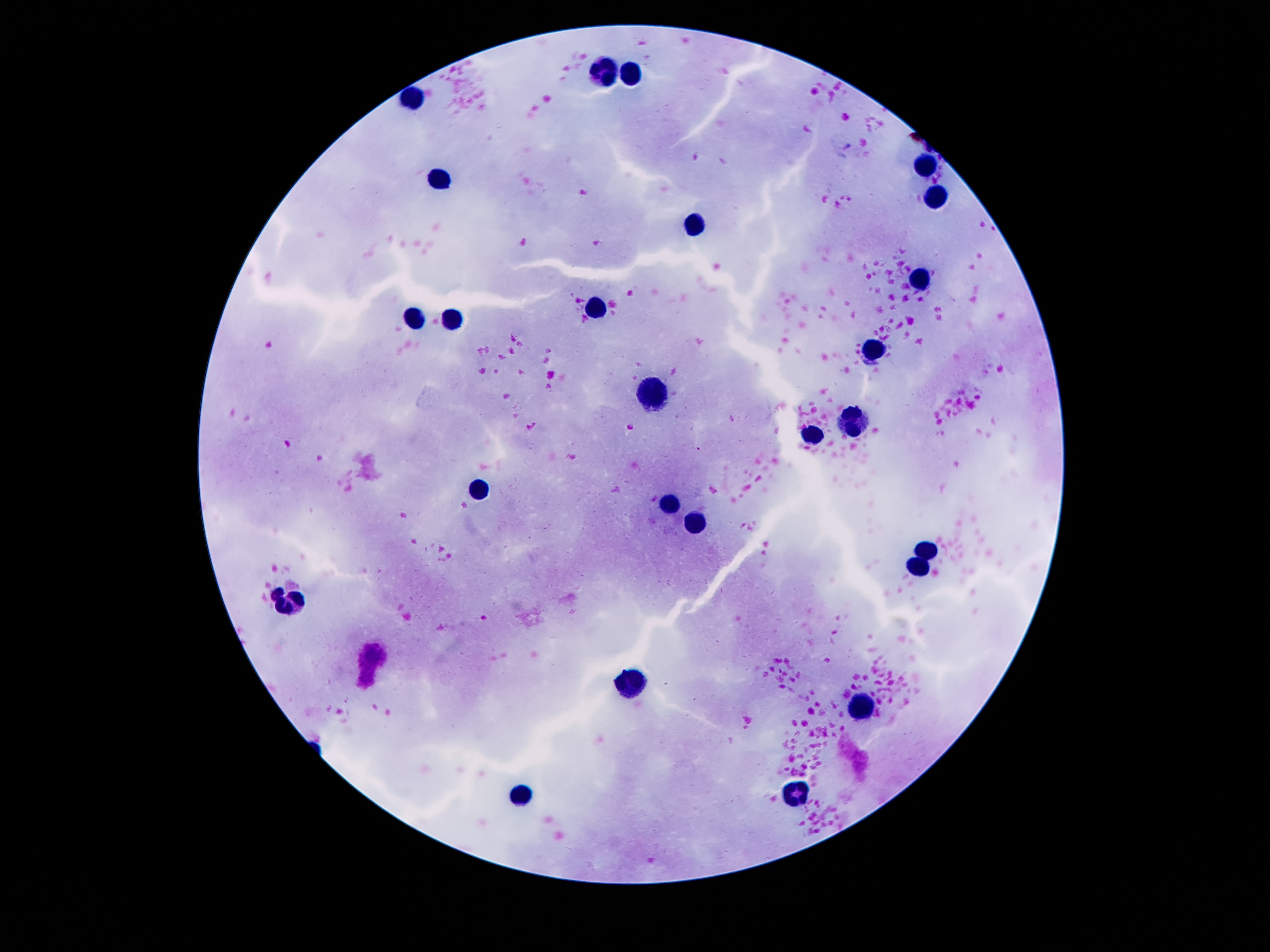
Approximate centers as [x, y] in pixels.
Summary:
  - Leukocyte locations: [604, 71], [633, 75], [412, 100], [926, 169], [443, 180], [938, 198], [695, 225], [922, 281], [594, 305], [410, 317], [453, 320], [875, 352], [652, 397], [854, 420], [811, 437], [481, 487], [672, 504], [695, 523], [926, 549], [920, 566], [287, 599], [629, 683], [863, 707], [797, 793], [522, 795]
  - Stain: Giemsa
  - Image size: 1270×952 pixels
  - Preparation: thick blood film
  - Capture: smartphone camera through the microscope eyepiece
  - Patient malaria status: negative
  - Field of view: one from this slide
  - Magnification: 100x